Identify the parasite.
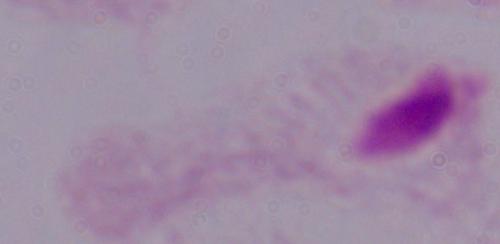

A trichomonad.

Photomicrograph. 1000x magnification.